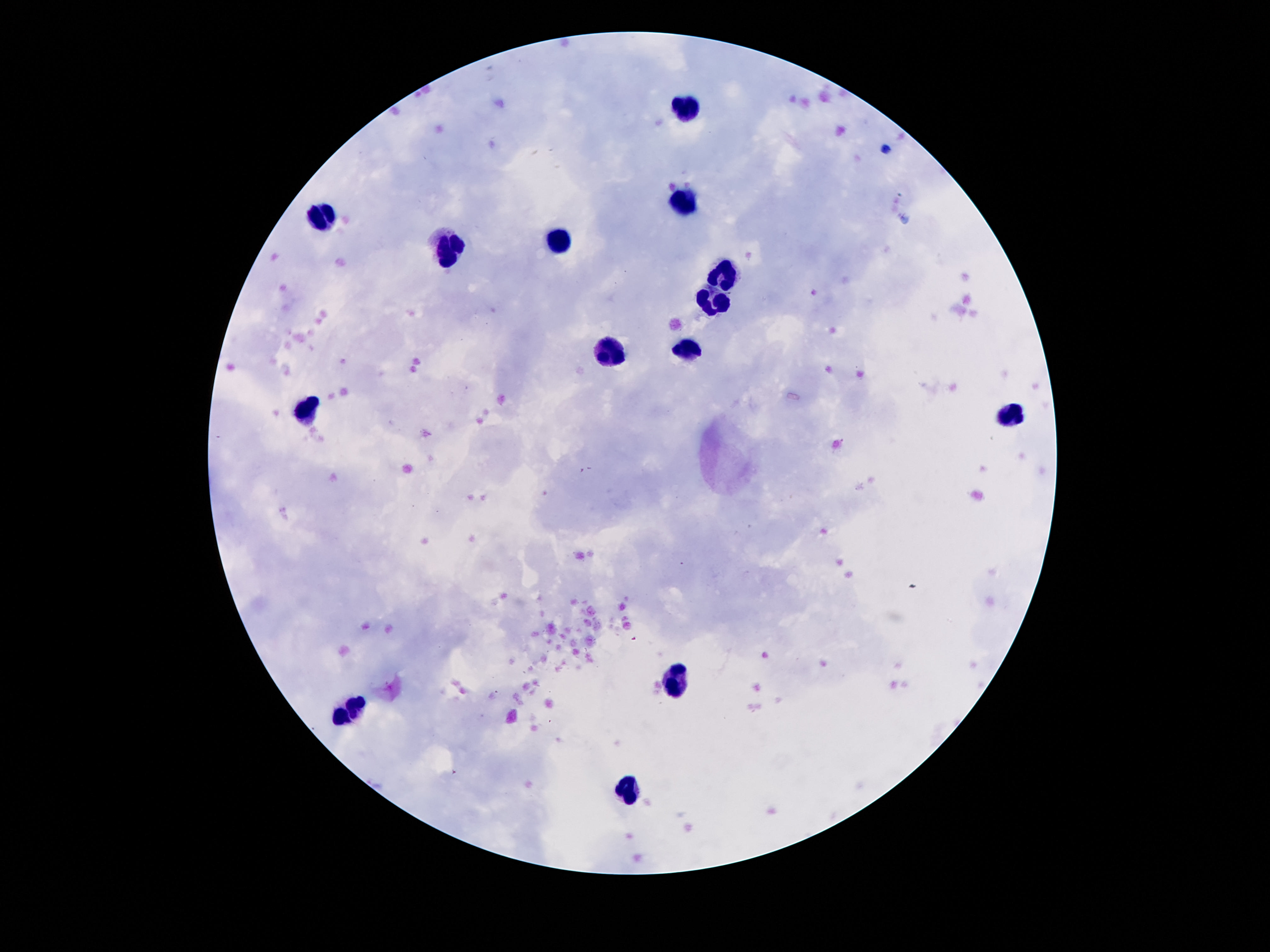

{
  "patient_malaria_status": "uninfected",
  "stain": "Giemsa",
  "capture": "smartphone camera through the microscope eyepiece",
  "field_of_view": "single",
  "leukocyte_locations": "approximate object centers, in pixels from the top-left corner: (x=683, y=105), (x=678, y=201), (x=318, y=215), (x=554, y=242), (x=450, y=251), (x=723, y=277), (x=711, y=301), (x=687, y=350), (x=612, y=354), (x=307, y=410), (x=1012, y=416), (x=676, y=677), (x=355, y=710), (x=625, y=790)",
  "image_size": "1270×952 pixels",
  "preparation": "thick blood smear",
  "magnification": "100x"
}